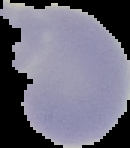

{
  "malaria_status": "uninfected",
  "image_size": "130×148 pixels",
  "preparation": "thin blood smear",
  "image_type": "cell region segmented out of the field of view; surrounding area masked to black"
}